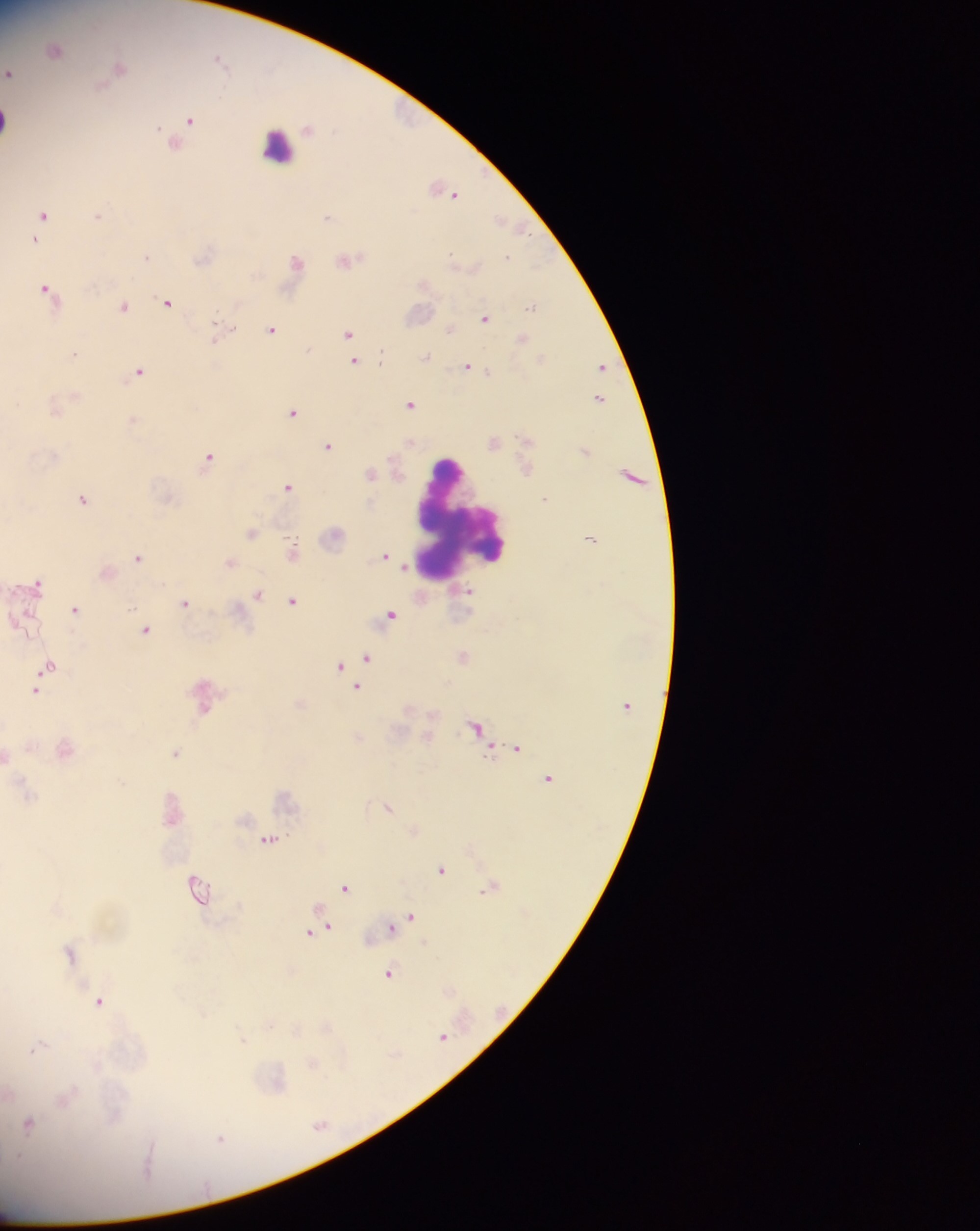
Approximate centers as (x, y) in pixels.
Summary:
  - Leukocyte locations: (6, 120), (277, 146), (461, 519)
  - Plasmodium parasite locations: (56, 50), (220, 58), (119, 67), (8, 73), (190, 119), (447, 191), (43, 214), (98, 216), (328, 216), (503, 221), (36, 239), (507, 256), (145, 257), (348, 259), (296, 261), (47, 288), (167, 303), (123, 306), (533, 306), (485, 318), (451, 329), (272, 330), (219, 332), (349, 333), (523, 339), (73, 354), (425, 358), (354, 362), (601, 366), (467, 367), (138, 372), (599, 398), (411, 404), (293, 413), (494, 443), (328, 446), (209, 459), (371, 474), (289, 487), (546, 498), (83, 499), (251, 533), (334, 538), (590, 538), (292, 550), (385, 555), (138, 557), (229, 562), (38, 583), (258, 595), (292, 600), (185, 604), (75, 609), (391, 615), (146, 630), (368, 657), (463, 657), (49, 666), (340, 666), (357, 688), (35, 691), (476, 727), (517, 748), (175, 753), (6, 756), (548, 778), (388, 807), (268, 839), (441, 869), (197, 886), (346, 887), (411, 917), (403, 921), (392, 927), (321, 929), (312, 932), (69, 952), (389, 973), (99, 1002), (327, 1026), (443, 1036), (243, 1039), (38, 1046), (314, 1064), (29, 1124), (320, 1126), (221, 1138)
  - Preparation: thick blood smear
  - Field of view: single
  - Country: Ghana
  - Image size: 980×1231 pixels
  - Capture: mobile-phone photograph through a microscope